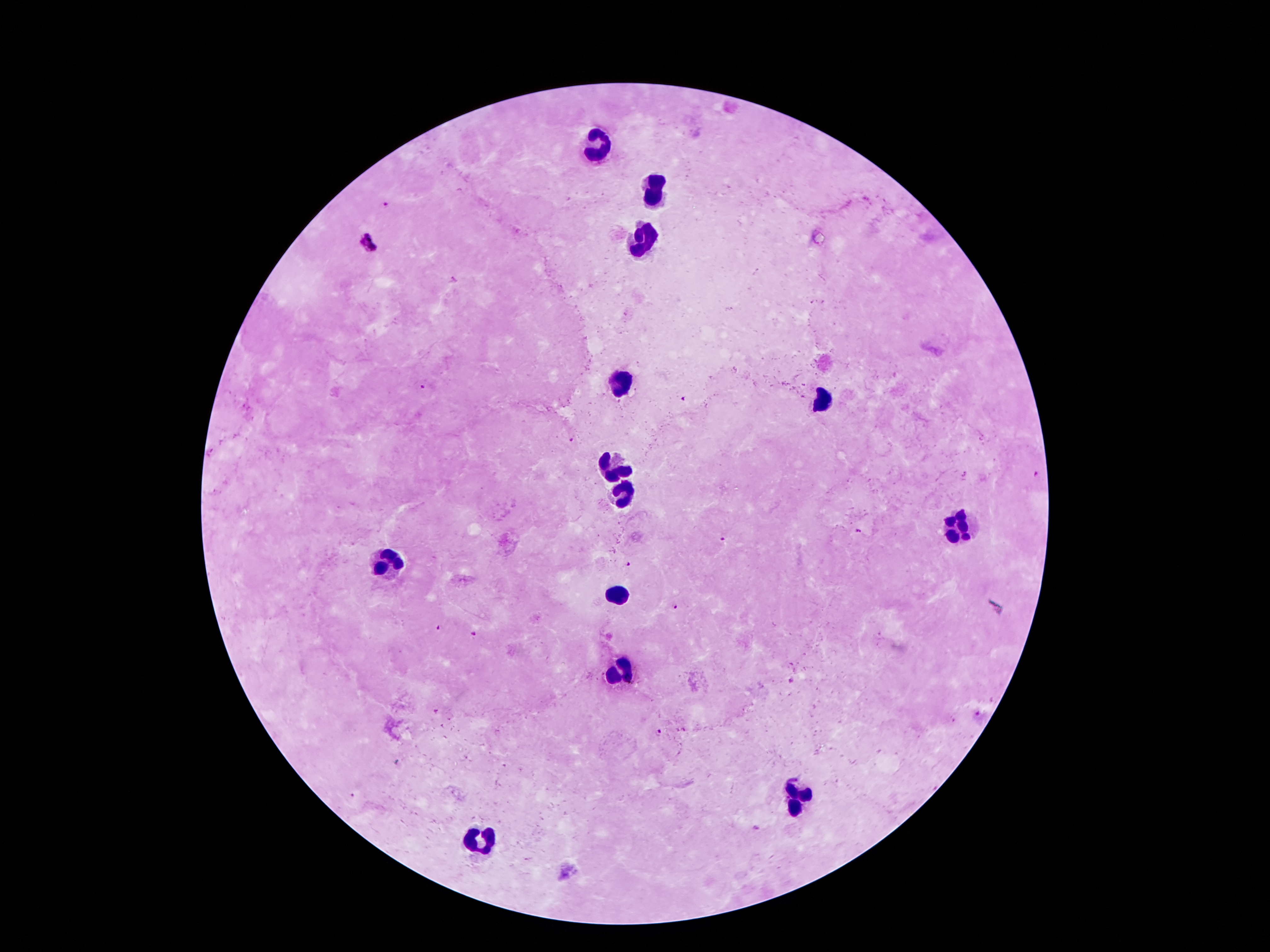
Approximate object centers, in pixels from the top-left corner. Malaria parasite locations: (x=385, y=203), (x=368, y=244), (x=454, y=280), (x=421, y=387), (x=684, y=400), (x=570, y=440), (x=1035, y=472), (x=858, y=531), (x=722, y=538), (x=628, y=563), (x=676, y=604), (x=438, y=626), (x=473, y=634), (x=791, y=681), (x=659, y=733). Leukocyte locations: (x=599, y=149), (x=652, y=186), (x=643, y=240), (x=621, y=387), (x=822, y=402), (x=619, y=464), (x=623, y=495), (x=959, y=527), (x=387, y=560), (x=619, y=594), (x=623, y=668), (x=798, y=801), (x=480, y=841). Giemsa stain. Patient malaria status: infected with Plasmodium falciparum. Single field of view. Image is 1270×952 pixels. 100x magnification. Photographed through the microscope eyepiece with a smartphone camera. Thick peripheral-blood smear.